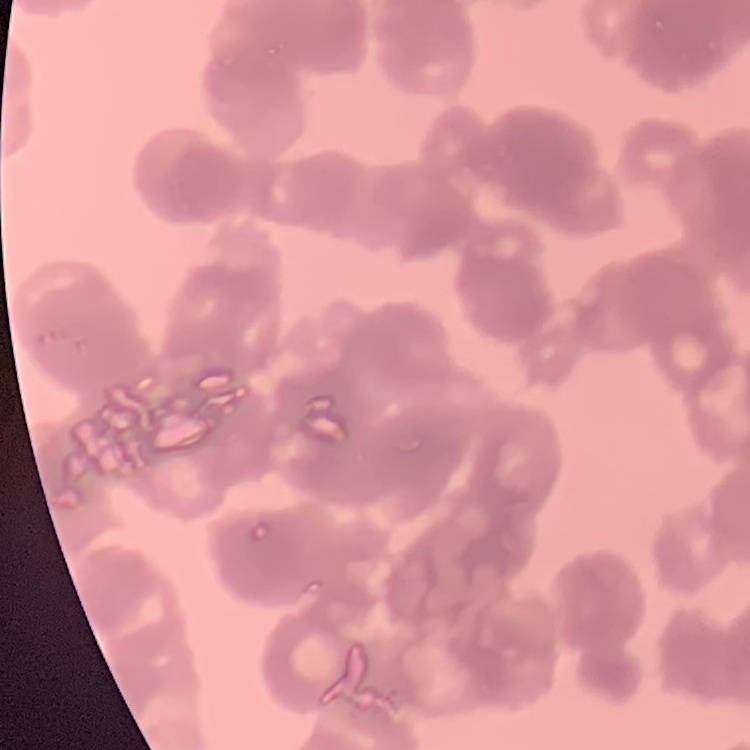

The erythrocytes exhibit rouleaux formation. One tile cut from a larger photomicrograph. Thin peripheral smear. Stained with either Field's or Giemsa.